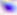

Summary:
  - Modality: photomicrograph
  - Identification: Toxoplasma gondii
  - Magnification: 400x